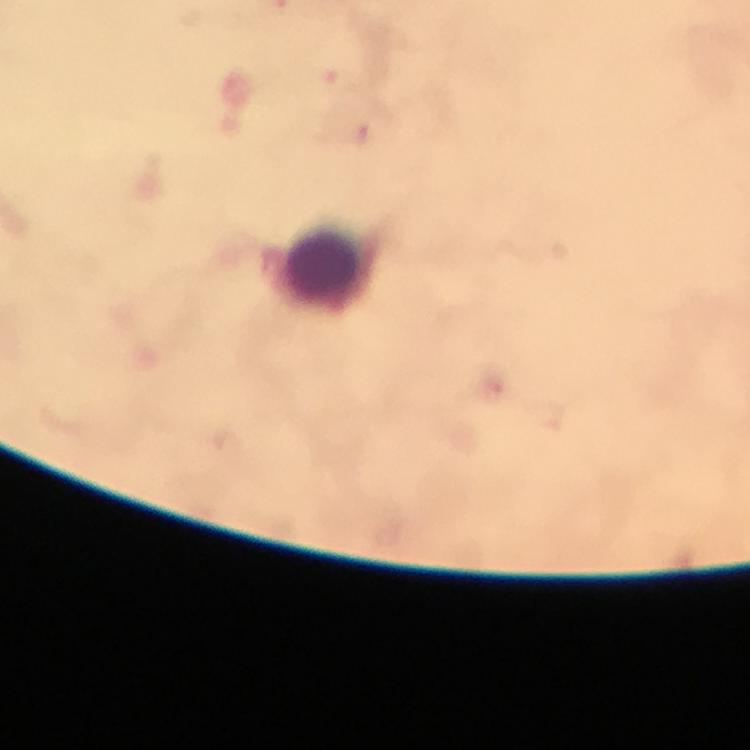

Approximate object centers, in pixels from the top-left corner.
Summary:
  - Malaria parasite locations: (x=491, y=388)
  - Leukocyte locations: (x=321, y=260)
  - Preparation: thick smear
  - Capture: smartphone mounted on the microscope
  - Image size: 750×750 pixels
  - Stain: Giemsa
  - Cropped from: one field of view
  - Immersion oil: used
  - Magnification: 100x
  - Context: from a malaria diagnostic workup